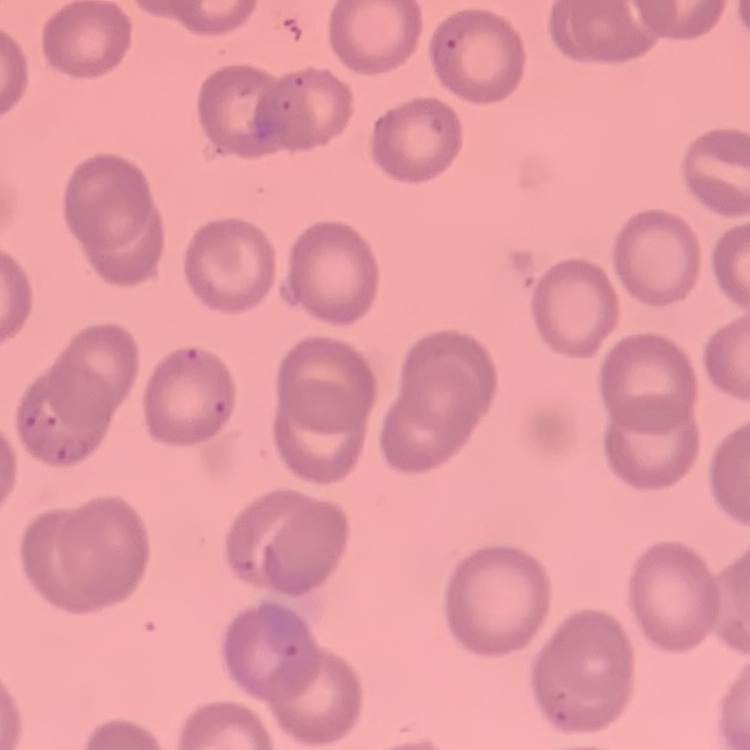
Summary:
  - Erythrocyte morphology: no rouleaux formation
  - Preparation: thin peripheral smear
  - Image type: square crop of a larger photomicrograph
  - Stain: Field's or Giemsa